Classify this cell by malaria status.
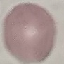
Uninfected.

Summary:
  - Capture: smartphone through the microscope eyepiece
  - Image type: automatically extracted cell patch, resized to 64 × 64 pixels
  - Stain: Giemsa
  - Preparation: thin blood smear